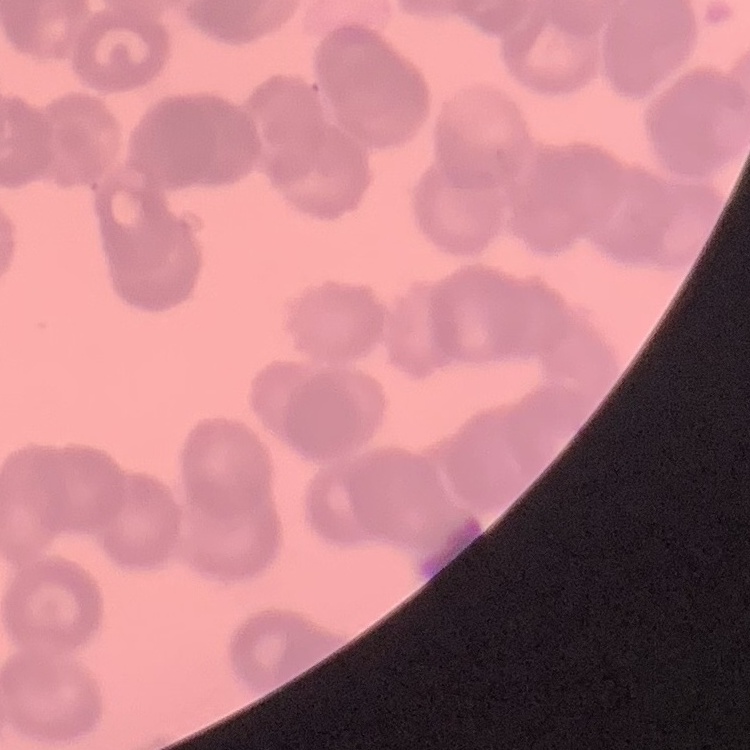 The erythrocytes exhibit rouleaux formation. Square crop of a larger photomicrograph. Stained with either Field's or Giemsa. Thin blood smear.